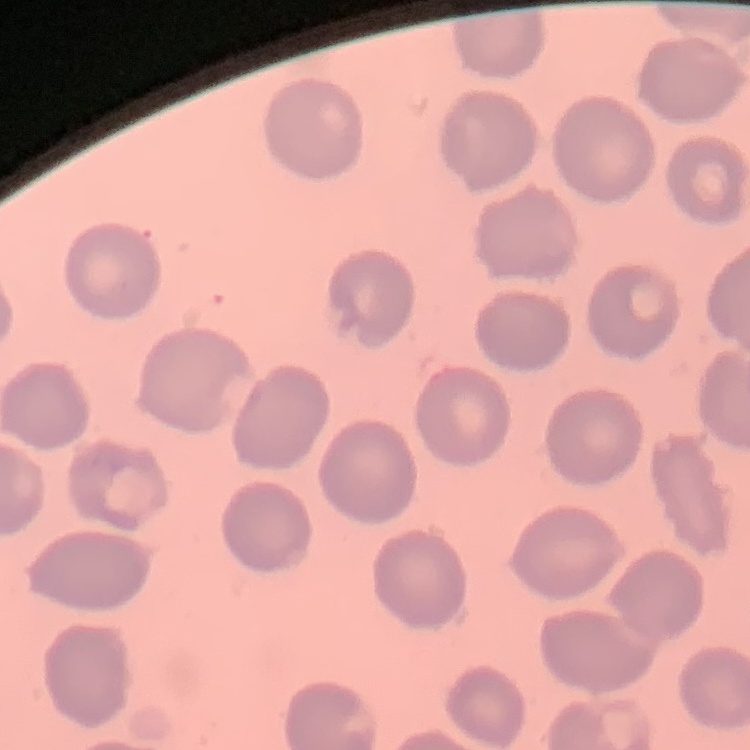

Summary:
  - Erythrocyte morphology: no rouleaux formation
  - Image type: one tile cut from a larger photomicrograph
  - Stain: Field's or Giemsa
  - Preparation: thin peripheral smear